Locate every leukocyte (white blood cell).
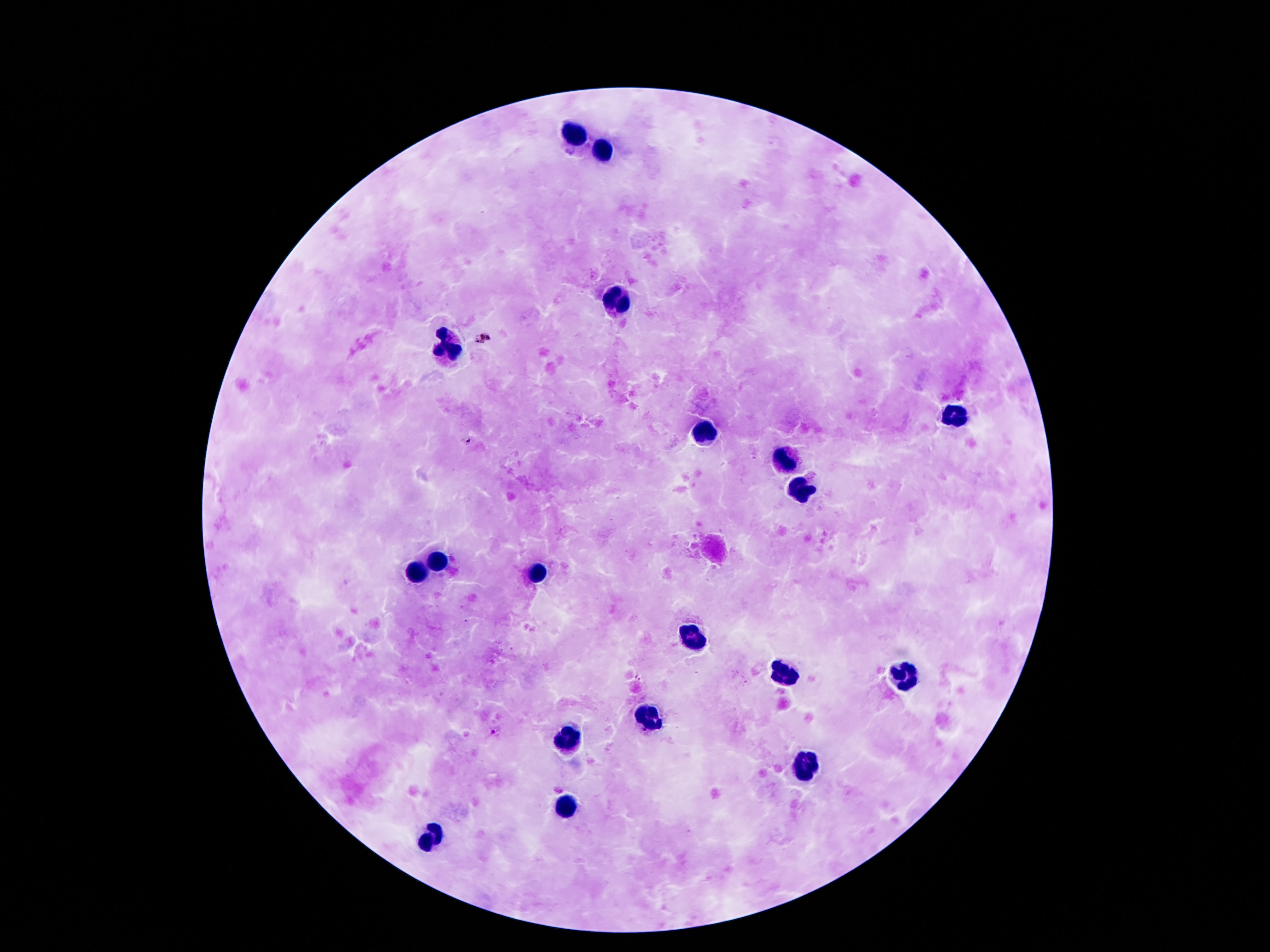
Approximate object centers, in pixels from the top-left corner.
Leukocytes: (x=575, y=134), (x=602, y=150), (x=616, y=299), (x=446, y=347), (x=954, y=418), (x=707, y=431), (x=783, y=461), (x=800, y=489), (x=438, y=562), (x=417, y=571), (x=536, y=574), (x=692, y=635), (x=786, y=672), (x=903, y=676), (x=649, y=716), (x=566, y=738), (x=810, y=766), (x=565, y=808), (x=431, y=839).

Summary:
  - Image size: 1270×952 pixels
  - Preparation: thick blood smear
  - Magnification: 100x
  - Patient malaria status: negative
  - Capture: smartphone camera through the microscope eyepiece
  - Field of view: one from this slide
  - Stain: Giemsa